Comment on the morphology of the erythrocytes.
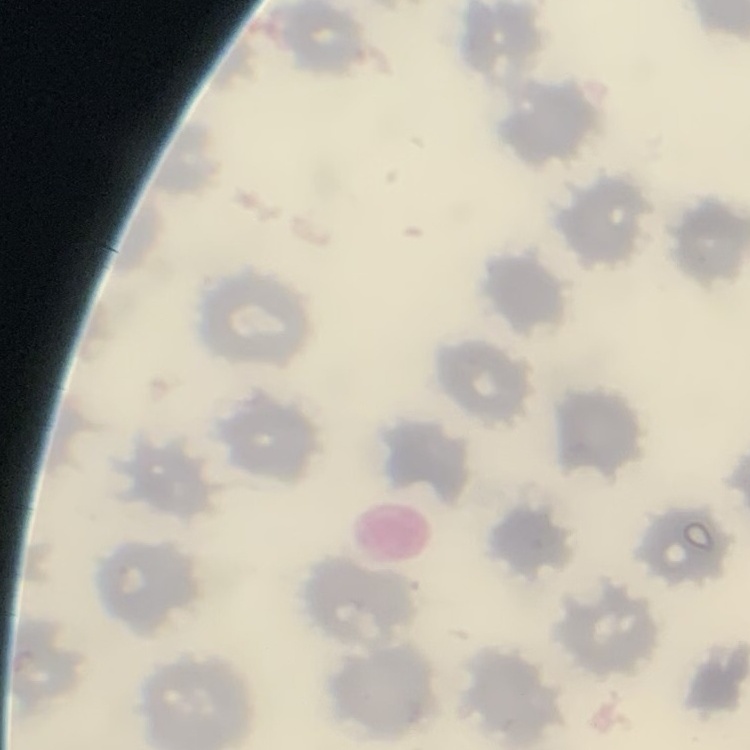

No rouleaux formation.

preparation = thin blood film
image type = one tile cut from a larger photomicrograph
stain = Field's or Giemsa